Locate every blood parasite and identify its species.
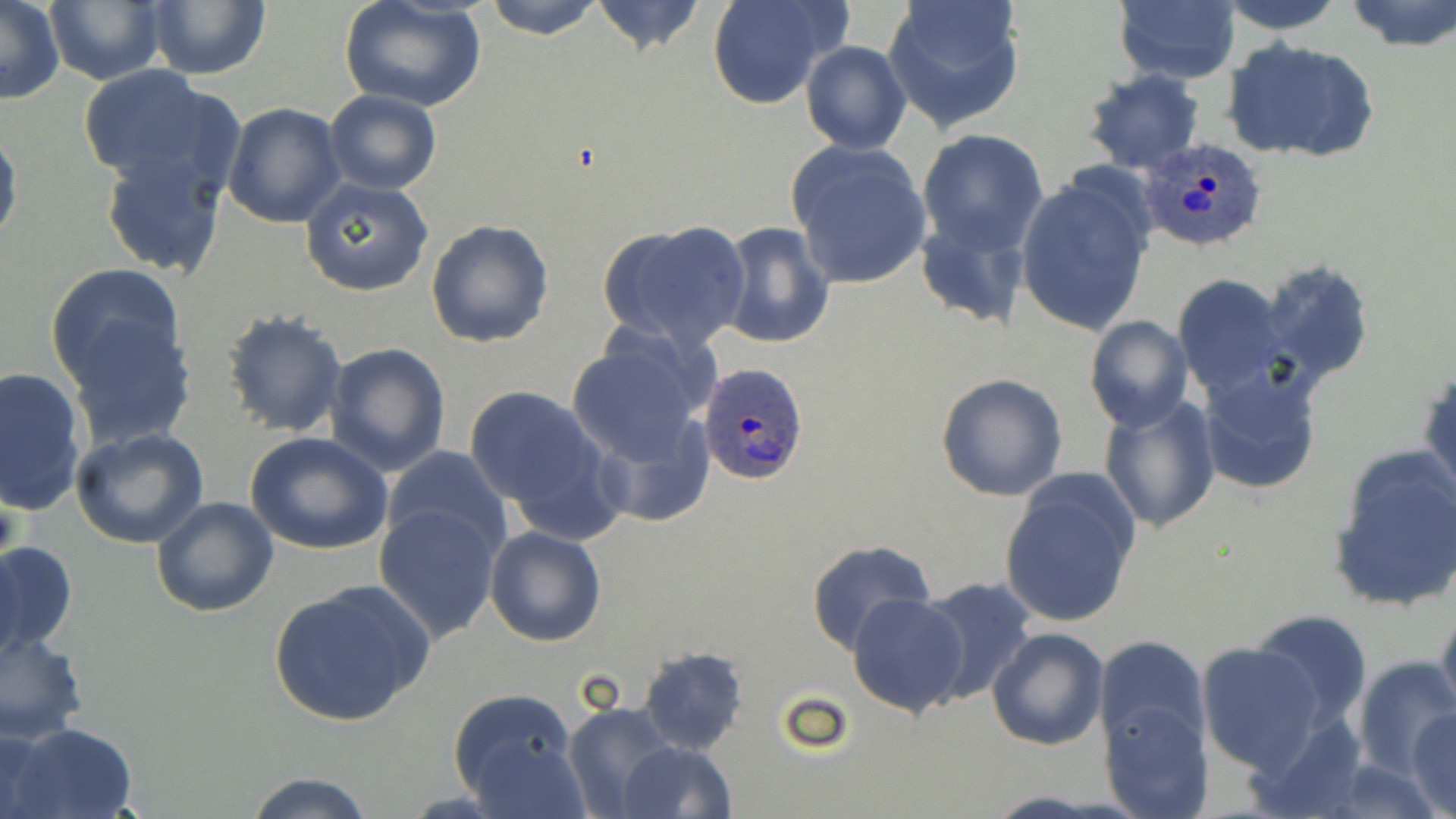

Approximate bounding boxes as named x1/y1/x2/y2 corners in pixels.
Plasmodium ovale-infected red blood cells: (x1=1139, y1=137, x2=1271, y2=252), (x1=699, y1=361, x2=808, y2=485).
No Plasmodium falciparum, Plasmodium malariae, Plasmodium vivax, Babesia divergens, or Trypanosoma brucei observed.

Summary:
  - Uninfected red blood cell locations: (x1=0, y1=0, x2=64, y2=105), (x1=42, y1=0, x2=166, y2=86), (x1=142, y1=0, x2=270, y2=81), (x1=337, y1=0, x2=488, y2=113), (x1=484, y1=0, x2=606, y2=41), (x1=589, y1=0, x2=708, y2=57), (x1=707, y1=0, x2=846, y2=110), (x1=881, y1=0, x2=1026, y2=134), (x1=1219, y1=0, x2=1346, y2=35), (x1=1345, y1=0, x2=1456, y2=52), (x1=1114, y1=1, x2=1241, y2=85), (x1=801, y1=39, x2=911, y2=155), (x1=1223, y1=40, x2=1379, y2=163), (x1=75, y1=65, x2=240, y2=197), (x1=1082, y1=69, x2=1205, y2=175), (x1=324, y1=89, x2=442, y2=194), (x1=223, y1=102, x2=347, y2=228), (x1=0, y1=120, x2=22, y2=255), (x1=918, y1=126, x2=1049, y2=254), (x1=787, y1=143, x2=933, y2=289), (x1=97, y1=145, x2=230, y2=279), (x1=1015, y1=176, x2=1154, y2=336), (x1=300, y1=178, x2=435, y2=296), (x1=915, y1=215, x2=1033, y2=331), (x1=425, y1=219, x2=553, y2=348), (x1=597, y1=221, x2=752, y2=352), (x1=717, y1=221, x2=834, y2=351), (x1=1259, y1=258, x2=1374, y2=389), (x1=45, y1=262, x2=186, y2=393), (x1=1173, y1=276, x2=1290, y2=398), (x1=218, y1=307, x2=349, y2=437), (x1=1084, y1=316, x2=1194, y2=433), (x1=62, y1=317, x2=197, y2=449), (x1=565, y1=337, x2=711, y2=468), (x1=324, y1=342, x2=451, y2=476), (x1=1420, y1=360, x2=1455, y2=507), (x1=1197, y1=363, x2=1323, y2=496), (x1=0, y1=365, x2=88, y2=518), (x1=937, y1=372, x2=1068, y2=502), (x1=464, y1=386, x2=608, y2=514), (x1=1097, y1=394, x2=1221, y2=535), (x1=588, y1=414, x2=713, y2=529), (x1=69, y1=427, x2=210, y2=549), (x1=245, y1=432, x2=393, y2=555), (x1=381, y1=446, x2=512, y2=557), (x1=1327, y1=446, x2=1456, y2=612), (x1=998, y1=472, x2=1141, y2=631), (x1=150, y1=496, x2=279, y2=618), (x1=375, y1=505, x2=503, y2=641), (x1=483, y1=526, x2=607, y2=647), (x1=0, y1=539, x2=79, y2=663), (x1=806, y1=539, x2=936, y2=653), (x1=913, y1=577, x2=1039, y2=703), (x1=270, y1=580, x2=431, y2=729), (x1=847, y1=593, x2=969, y2=718), (x1=1436, y1=603, x2=1456, y2=726), (x1=1250, y1=608, x2=1374, y2=731), (x1=989, y1=627, x2=1108, y2=749), (x1=1, y1=630, x2=88, y2=744), (x1=1094, y1=635, x2=1209, y2=757), (x1=1196, y1=641, x2=1326, y2=774), (x1=637, y1=646, x2=749, y2=754), (x1=1352, y1=654, x2=1455, y2=778), (x1=448, y1=690, x2=582, y2=806), (x1=563, y1=700, x2=681, y2=817), (x1=1103, y1=701, x2=1212, y2=818), (x1=1409, y1=708, x2=1456, y2=818), (x1=1240, y1=710, x2=1375, y2=819), (x1=9, y1=723, x2=138, y2=818), (x1=1, y1=727, x2=56, y2=817), (x1=467, y1=738, x2=590, y2=817), (x1=617, y1=739, x2=736, y2=819), (x1=240, y1=773, x2=381, y2=819)
  - Slide-level diagnosis: Plasmodium ovale
  - Preparation: thin blood film
  - Stain: May-Grünwald-Giemsa
  - Modality: light microscopy
  - Image size: 1456×819 pixels
  - Magnification: 1000x
  - Field of view: one of a larger specimen